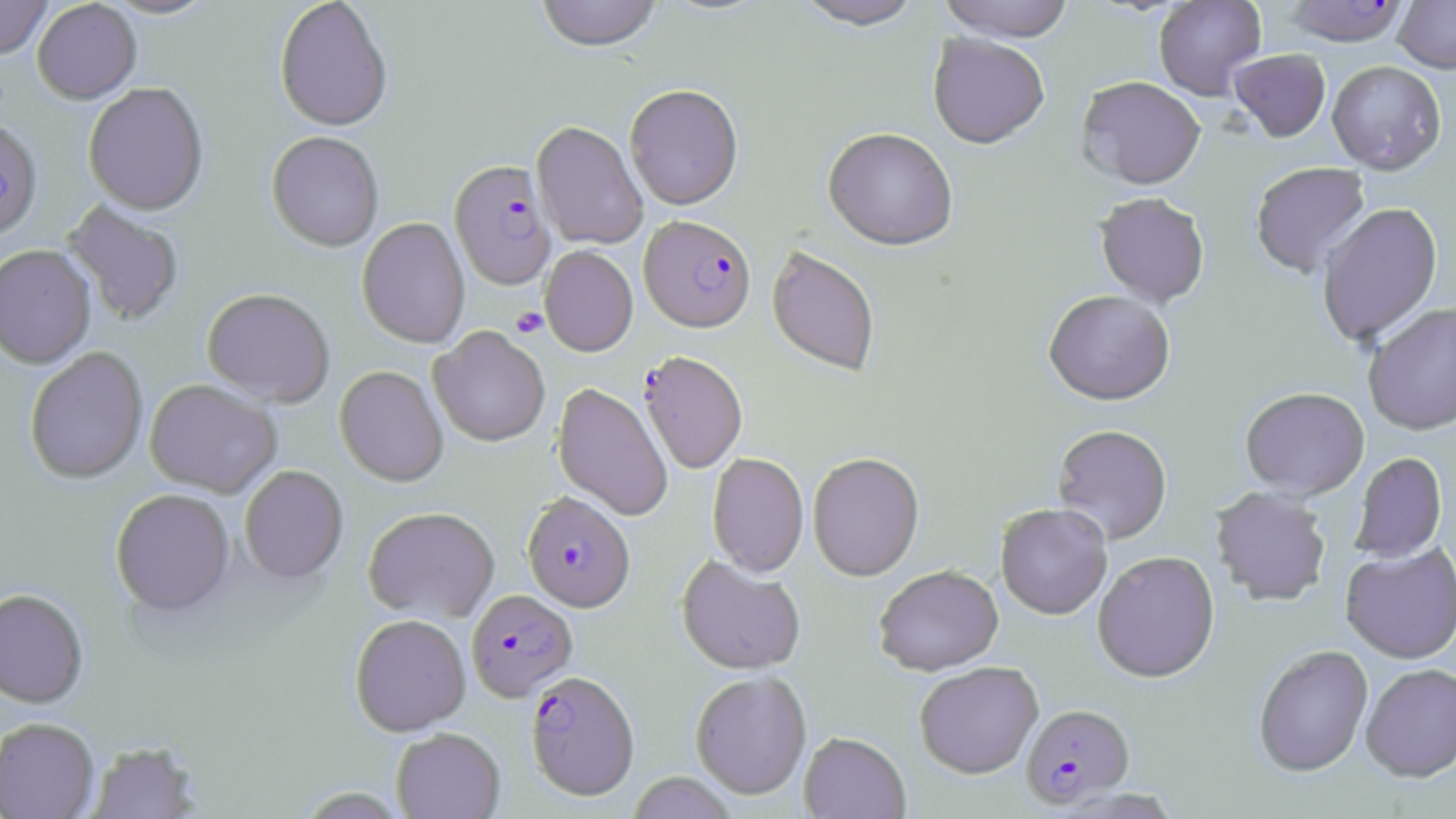
slide-level diagnosis = Plasmodium falciparum
modality = optical microscopy
field of view = single
image size = 1456×819 pixels
stain = May-Grünwald-Giemsa
Plasmodium falciparum-infected red blood cell locations = approximate bounding boxes as [x1, y1, x2, y2] in pixels: [1281, 1, 1410, 48], [0, 122, 43, 243], [449, 163, 556, 293], [640, 213, 757, 332], [639, 352, 747, 475], [522, 494, 636, 615], [466, 590, 578, 704], [526, 672, 640, 801], [1020, 705, 1135, 810]
preparation = thin blood film
uninfected red blood cell locations = approximate bounding boxes as [x1, y1, x2, y2] in pixels: [0, 0, 52, 61], [98, 0, 220, 21], [535, 0, 663, 55], [794, 0, 926, 34], [937, 0, 1075, 44], [1153, 0, 1267, 102], [32, 1, 142, 106], [275, 1, 393, 135], [1393, 1, 1456, 75], [927, 36, 1049, 152], [1229, 50, 1331, 144], [1327, 62, 1446, 178], [1076, 79, 1206, 193], [84, 85, 208, 218], [625, 87, 743, 213], [531, 123, 648, 252], [822, 130, 957, 254], [266, 133, 384, 254], [1251, 164, 1371, 280], [1095, 195, 1209, 309], [61, 201, 185, 327], [1317, 205, 1444, 349], [356, 219, 470, 350], [0, 246, 96, 370], [540, 247, 638, 358], [766, 247, 880, 379], [201, 291, 335, 409], [1043, 293, 1174, 409], [1364, 305, 1456, 438], [429, 328, 550, 448], [24, 348, 149, 485], [335, 367, 448, 488], [144, 381, 282, 498], [552, 384, 672, 522], [1240, 390, 1370, 503], [1052, 426, 1172, 546], [707, 454, 808, 579], [808, 454, 924, 583], [1350, 454, 1447, 564], [240, 466, 348, 585], [1210, 489, 1331, 608], [110, 490, 235, 619], [995, 506, 1112, 622], [362, 509, 500, 624], [1340, 545, 1455, 666], [1092, 553, 1220, 686], [675, 557, 805, 676], [874, 567, 1004, 678], [0, 590, 89, 710], [350, 616, 472, 737], [1253, 647, 1373, 780], [915, 664, 1044, 780], [1360, 665, 1456, 786], [690, 673, 812, 801], [0, 719, 99, 819], [391, 729, 506, 819], [798, 734, 911, 819], [86, 742, 201, 819], [626, 772, 739, 819]
magnification = 1000x
platelet locations = approximate bounding boxes as [x1, y1, x2, y2] in pixels: [511, 308, 547, 338]